Classify this cell by malaria status.
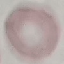
Uninfected.

image type = automatically extracted cell patch, resized to 64 × 64 pixels
stain = Giemsa
capture = smartphone through the microscope eyepiece
preparation = thin blood film